Point out each leukocyte.
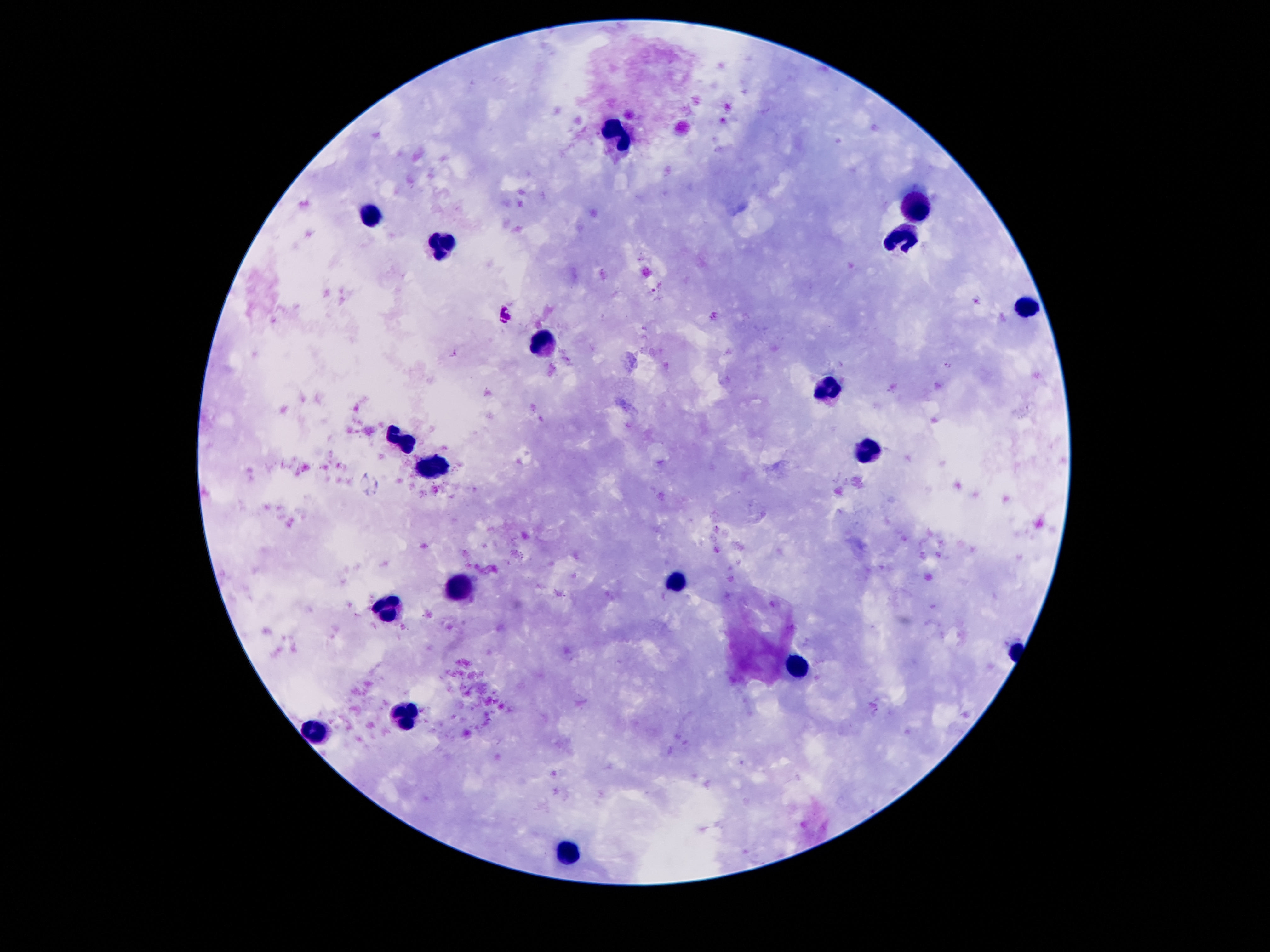

Approximate centers as (x, y) in pixels.
Leukocytes: (619, 134), (914, 209), (374, 216), (905, 243), (442, 247), (1026, 309), (540, 341), (828, 386), (400, 441), (862, 450), (434, 465), (679, 581), (458, 586), (388, 609), (797, 670), (404, 715), (318, 734), (569, 851).

Summary:
  - Preparation: thick blood film
  - Image size: 1270×952 pixels
  - Patient malaria status: negative
  - Magnification: 100x
  - Stain: Giemsa
  - Capture: smartphone camera through the microscope eyepiece
  - Field of view: single